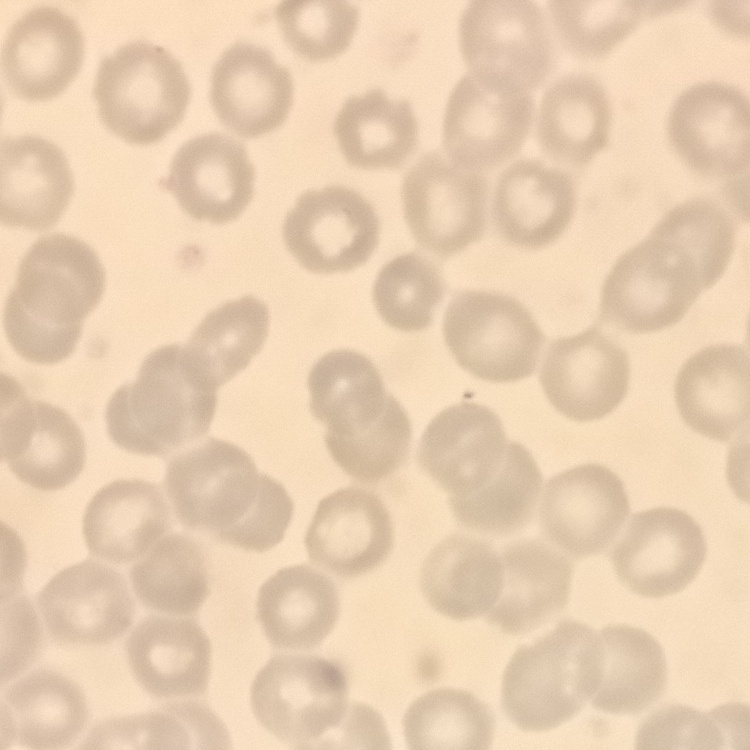
The red blood cells show no rouleaux formation. Square crop of a larger photomicrograph. Stained with either Field's or Giemsa. Thin blood smear.